Comment on the morphology of the erythrocytes.
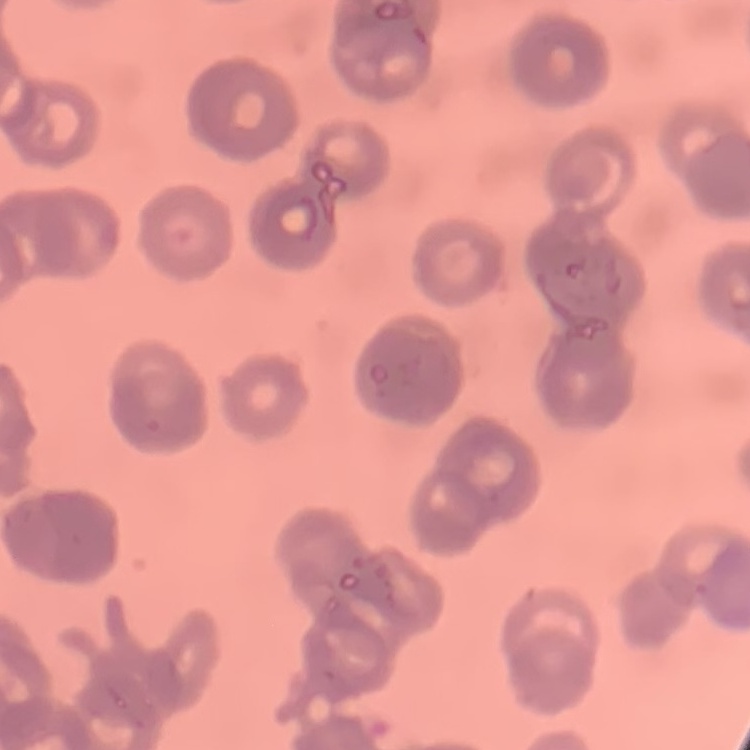
They show rouleaux formation.

{
  "image_type": "one tile cut from a larger photomicrograph",
  "stain": "Field's or Giemsa",
  "preparation": "thin blood film"
}